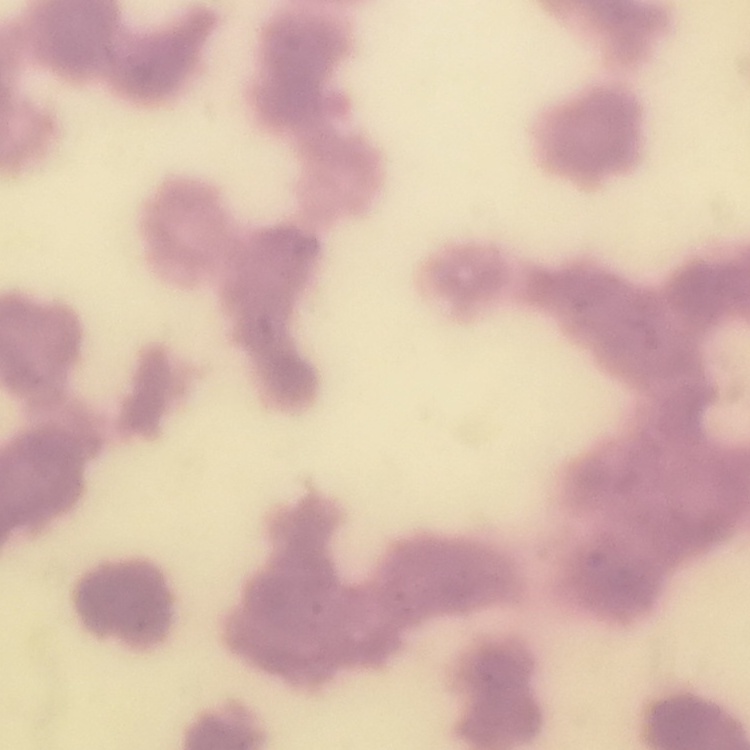
Summary:
  - Red blood cell morphology: rouleaux formation
  - Stain: Field's or Giemsa
  - Preparation: thin blood smear
  - Image type: square crop of a larger photomicrograph